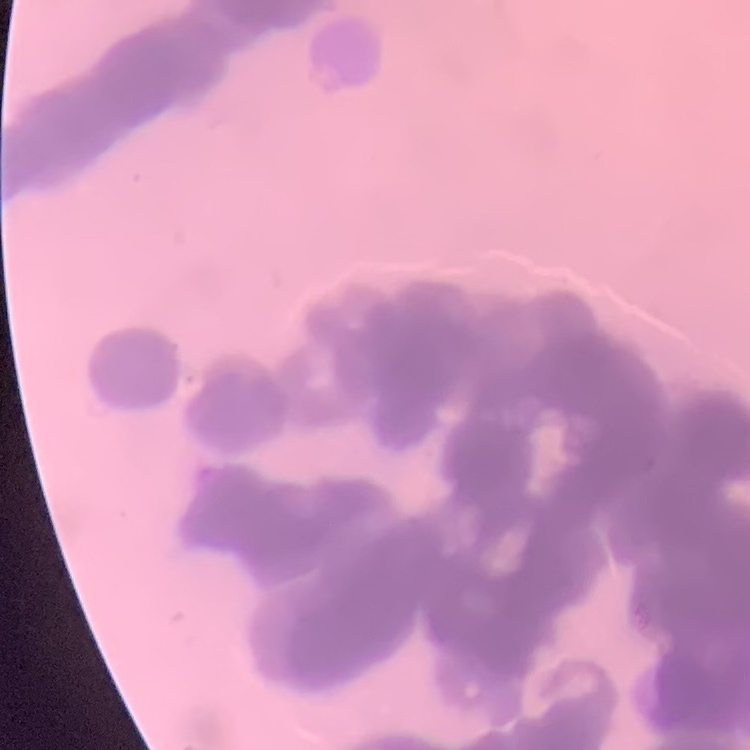 The erythrocytes exhibit rouleaux formation. Thin blood smear. Stained with either Field's or Giemsa. Square crop of a larger photomicrograph.